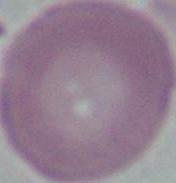 1000x magnification. Photomicrograph. A red blood cell is shown.